Outline each blood parasite and name the species.
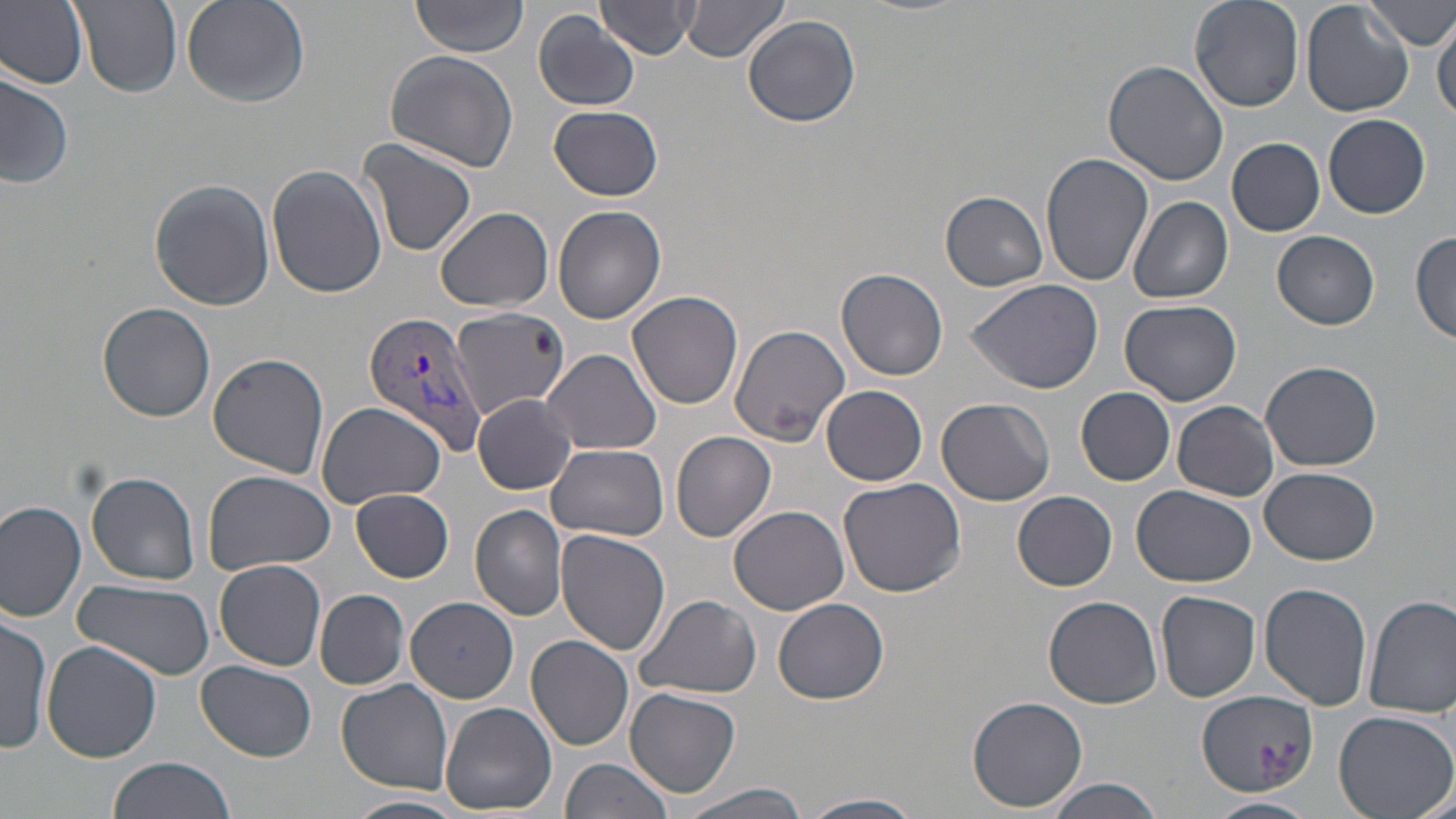

Approximate bounding boxes as (x1,y1)-(x2,y2) corner pairs in pixels.
Plasmodium vivax-infected red blood cells: (363,312)-(486,454).
No Plasmodium falciparum, Plasmodium ovale, Plasmodium malariae, Babesia divergens, or Trypanosoma brucei observed.

slide_level_diagnosis: Plasmodium vivax
magnification: 1000x
image_size: 1456×819 pixels
stain: May-Grünwald-Giemsa
field_of_view: single
preparation: thin blood film
uninfected_red_blood_cell_locations: 'approximate bounding boxes as (x1,y1)-(x2,y2) corner pairs in pixels: (75,0)-(181,96), (181,0)-(312,108), (412,0)-(528,57), (600,0)-(700,57), (1188,0)-(1302,111), (1299,0)-(1413,118), (1367,0)-(1456,50), (0,1)-(89,90), (681,1)-(790,65), (533,11)-(639,111), (1433,12)-(1455,122), (743,15)-(860,128), (383,49)-(519,172), (1102,60)-(1230,186), (0,69)-(73,191), (550,106)-(663,202), (1324,113)-(1431,218), (1227,137)-(1326,237), (358,138)-(477,259), (1040,151)-(1154,287), (268,166)-(386,298), (149,179)-(274,310), (941,190)-(1050,291), (1128,195)-(1234,303), (553,204)-(667,324), (435,206)-(556,312), (1410,228)-(1456,345), (1271,229)-(1380,328), (837,268)-(950,382), (966,277)-(1103,393), (628,290)-(744,409), (1120,298)-(1241,407), (98,301)-(217,421), (450,306)-(568,418), (730,325)-(848,443), (540,349)-(662,455), (207,353)-(329,479), (1260,361)-(1382,470), (822,385)-(928,487), (1076,386)-(1175,486), (474,394)-(579,495), (937,397)-(1055,505), (314,401)-(446,508), (1173,402)-(1279,500), (671,430)-(777,542), (548,443)-(669,541), (1258,467)-(1380,565), (203,470)-(335,574), (86,472)-(200,584), (837,477)-(967,600), (1131,485)-(1258,588), (351,489)-(454,582), (1013,491)-(1117,591), (0,502)-(87,623), (470,504)-(568,621), (729,506)-(851,615), (556,530)-(670,658), (213,559)-(327,672), (73,579)-(217,679), (1259,583)-(1373,710), (315,589)-(409,689), (1155,591)-(1260,704), (1363,594)-(1456,718), (635,595)-(764,699), (1043,595)-(1162,708), (406,596)-(519,703), (774,598)-(888,705), (0,616)-(52,752), (525,635)-(634,751), (43,641)-(161,764), (195,660)-(317,761), (337,679)-(453,794), (624,686)-(741,797), (1198,690)-(1318,794), (966,692)-(1090,812), (443,702)-(557,816), (1332,708)-(1456,818), (107,755)-(238,819), (560,757)-(676,819), (1044,777)-(1164,819), (674,782)-(816,819), (802,792)-(926,819), (347,793)-(469,819), (1206,796)-(1317,819)'
modality: light microscopy